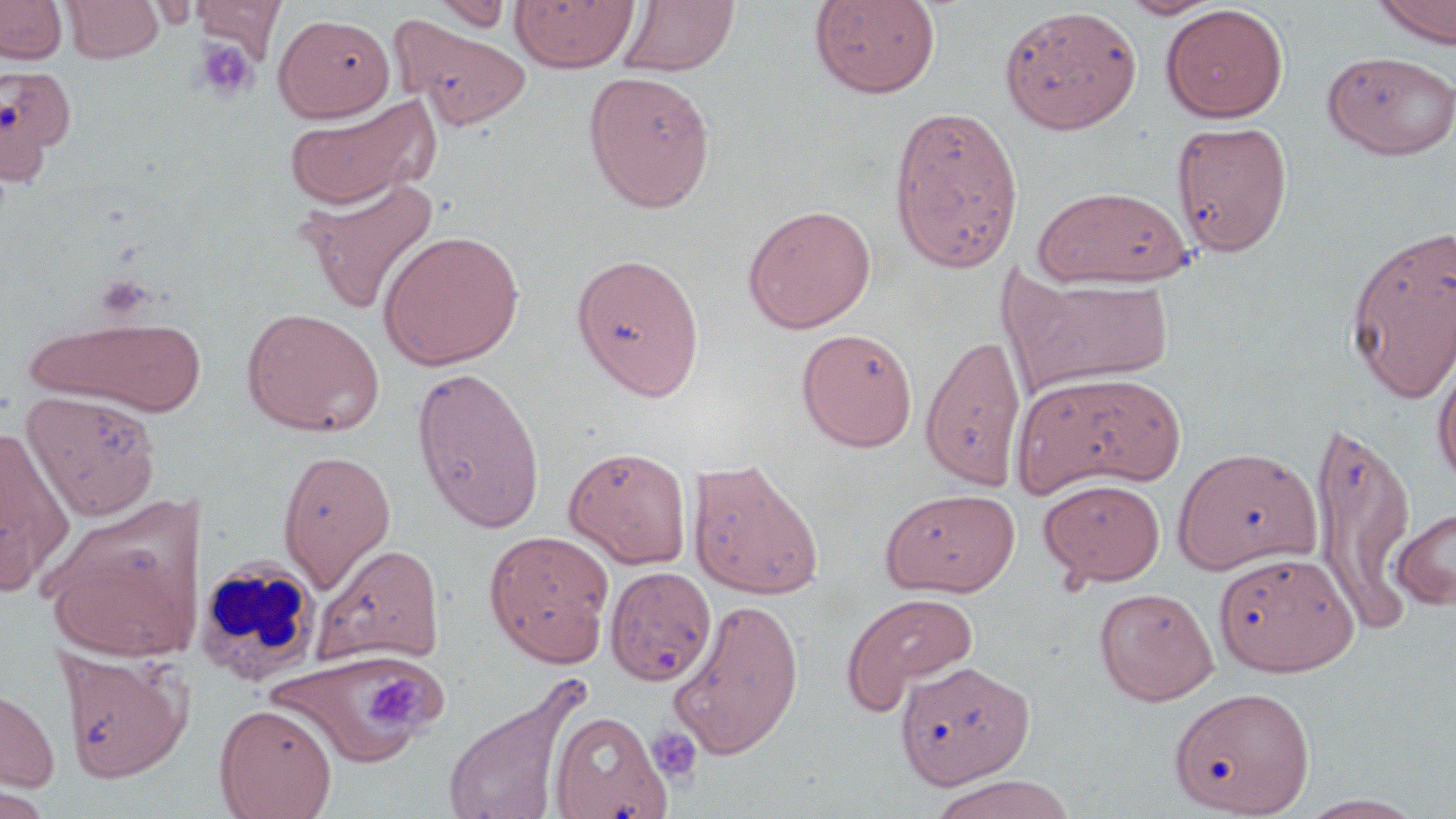

slide-level diagnosis = negative for blood parasites
platelet locations = approximate bounding boxes as [x1, y1, x2, y2] in pixels: [195, 39, 259, 102], [368, 674, 422, 725], [646, 726, 702, 784]
uninfected red blood cell locations = approximate bounding boxes as [x1, y1, x2, y2] in pixels: [0, 0, 67, 64], [62, 0, 163, 63], [192, 0, 287, 61], [428, 0, 514, 32], [510, 0, 640, 73], [809, 0, 940, 98], [1116, 0, 1227, 19], [1374, 0, 1456, 48], [619, 1, 739, 77], [1160, 4, 1288, 123], [999, 5, 1142, 135], [273, 13, 396, 122], [389, 15, 531, 133], [1322, 49, 1456, 160], [0, 62, 76, 183], [583, 70, 716, 212], [282, 94, 439, 210], [888, 105, 1024, 273], [1171, 119, 1293, 257], [299, 175, 440, 315], [1031, 185, 1194, 288], [742, 204, 877, 333], [1344, 223, 1456, 403], [378, 229, 524, 369], [571, 251, 705, 400], [1000, 271, 1175, 394], [242, 307, 385, 436], [25, 314, 209, 418], [796, 328, 918, 451], [920, 332, 1026, 490], [1432, 346, 1456, 485], [410, 364, 546, 533], [1013, 370, 1188, 495], [21, 389, 161, 520], [1308, 418, 1419, 626], [0, 422, 75, 596], [564, 445, 692, 568], [1173, 447, 1322, 574], [278, 448, 396, 591], [687, 458, 824, 600], [1039, 478, 1165, 587], [880, 488, 1020, 596], [42, 496, 204, 660], [1391, 504, 1456, 610], [484, 529, 615, 666], [313, 542, 446, 666], [1214, 551, 1357, 675], [605, 566, 718, 687], [1094, 586, 1219, 706], [841, 592, 979, 713], [668, 597, 804, 761], [56, 648, 193, 782], [266, 650, 434, 768], [896, 661, 1034, 789], [439, 676, 590, 819], [0, 680, 60, 794], [1168, 685, 1316, 818], [214, 703, 338, 819], [549, 710, 671, 819], [926, 774, 1076, 819], [1296, 794, 1428, 818]
modality = light microscopy
image size = 1456×819 pixels
magnification = 1000x
field of view = one of a larger specimen
preparation = thin blood film
stain = May-Grünwald-Giemsa
white blood cell locations = approximate bounding boxes as [x1, y1, x2, y2] in pixels: [195, 556, 323, 687]